Report the malaria status of this cell.
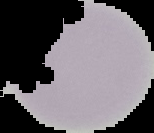

Uninfected.

From a thin blood film. Image is 154×133 pixels. Cell region segmented out of the field of view; the surrounding area is masked to black.